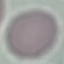

Result: negative for malaria parasites. Thin blood film. Photographed with a smartphone camera at the microscope eyepiece. Giemsa stain. Cell patch, automatically extracted from a larger field of view and resized to 64 × 64 pixels.